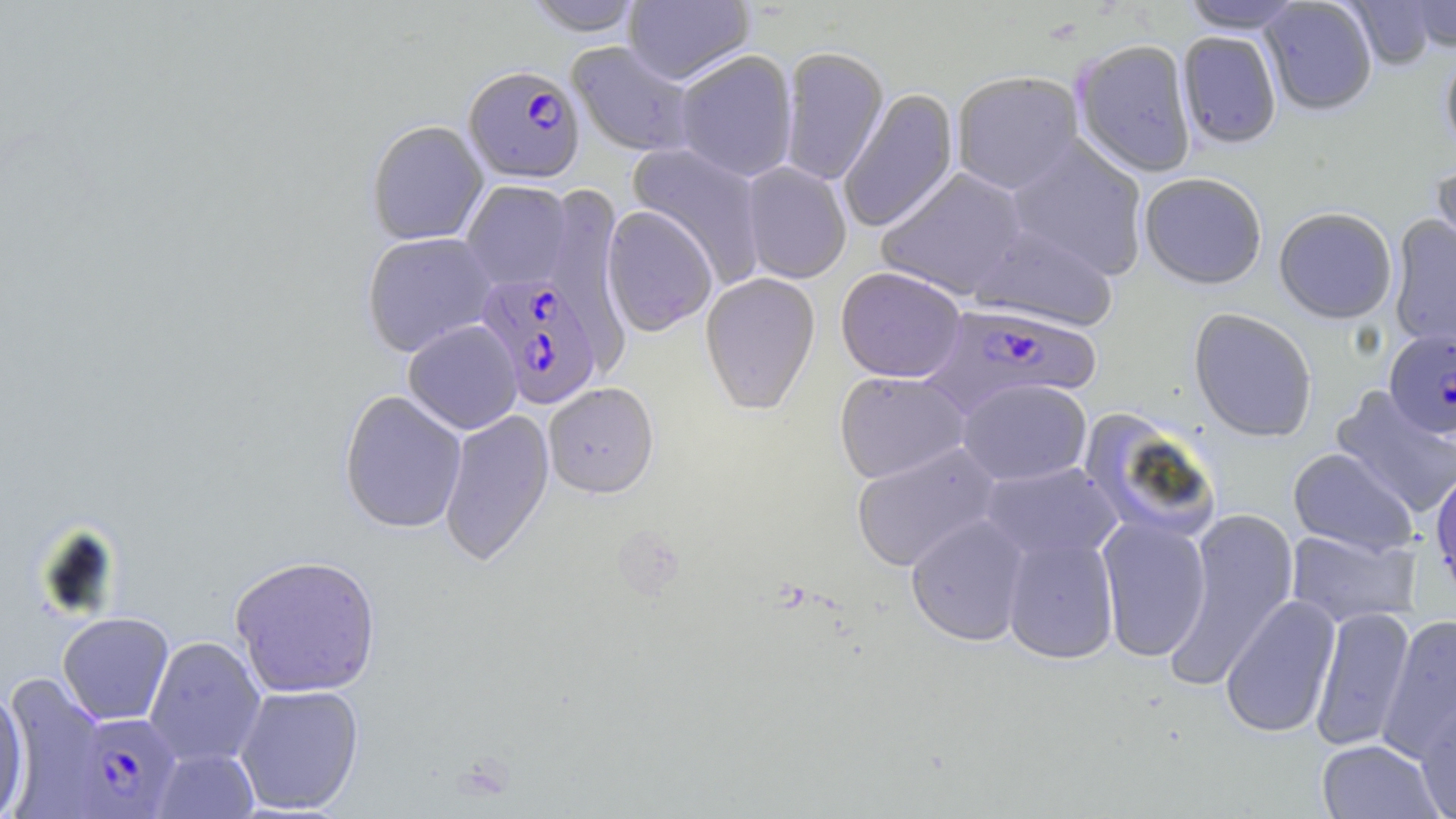
Summary:
  - Coordinate format: approximate bounding boxes as (x1, y1, x2, y2) in pixels
  - Plasmodium falciparum-infected red blood cell locations: (463, 64, 585, 182), (476, 272, 603, 408), (921, 302, 1102, 416), (1384, 329, 1456, 438), (74, 711, 181, 816)
  - Uninfected red blood cell locations: (523, 0, 645, 36), (623, 0, 754, 85), (1260, 0, 1377, 116), (1343, 0, 1441, 70), (1401, 0, 1455, 52), (1181, 1, 1304, 32), (1177, 31, 1282, 149), (1073, 39, 1197, 177), (566, 41, 697, 159), (1440, 44, 1456, 158), (779, 46, 889, 187), (674, 50, 798, 183), (951, 71, 1083, 194), (838, 89, 958, 233), (366, 120, 488, 246), (1006, 136, 1149, 282), (629, 143, 767, 287), (1430, 158, 1456, 272), (741, 162, 851, 284), (876, 166, 1029, 301), (1139, 172, 1267, 289), (461, 180, 573, 289), (541, 180, 631, 369), (602, 205, 718, 336), (1273, 206, 1398, 323), (1388, 214, 1456, 353), (970, 225, 1119, 332), (362, 231, 498, 357), (835, 266, 966, 383), (700, 272, 820, 414), (1188, 307, 1317, 442), (403, 320, 523, 434), (834, 370, 970, 483), (957, 378, 1092, 486), (543, 382, 659, 498), (1332, 387, 1456, 517), (339, 389, 467, 534), (439, 409, 554, 566), (1078, 409, 1221, 541), (851, 442, 1003, 572), (1288, 447, 1418, 556), (980, 462, 1123, 565), (1430, 463, 1456, 600), (1164, 508, 1299, 689), (906, 514, 1030, 646), (1096, 516, 1212, 662), (1286, 528, 1420, 629), (1003, 534, 1119, 664), (230, 553, 381, 698), (1220, 594, 1341, 739), (1310, 606, 1415, 751), (57, 612, 174, 724), (1377, 613, 1456, 762), (144, 636, 266, 768), (4, 672, 107, 817), (234, 684, 364, 814), (0, 688, 28, 817), (1415, 697, 1456, 818), (1315, 739, 1443, 819), (153, 747, 259, 818)
  - Slide-level diagnosis: Plasmodium falciparum
  - Field of view: one of a larger specimen
  - Preparation: thin blood smear
  - Image size: 1456×819 pixels
  - Stain: May-Grünwald-Giemsa
  - Modality: light microscopy
  - Magnification: 1000x